Locate every Plasmodium falciparum-infected red blood cell.
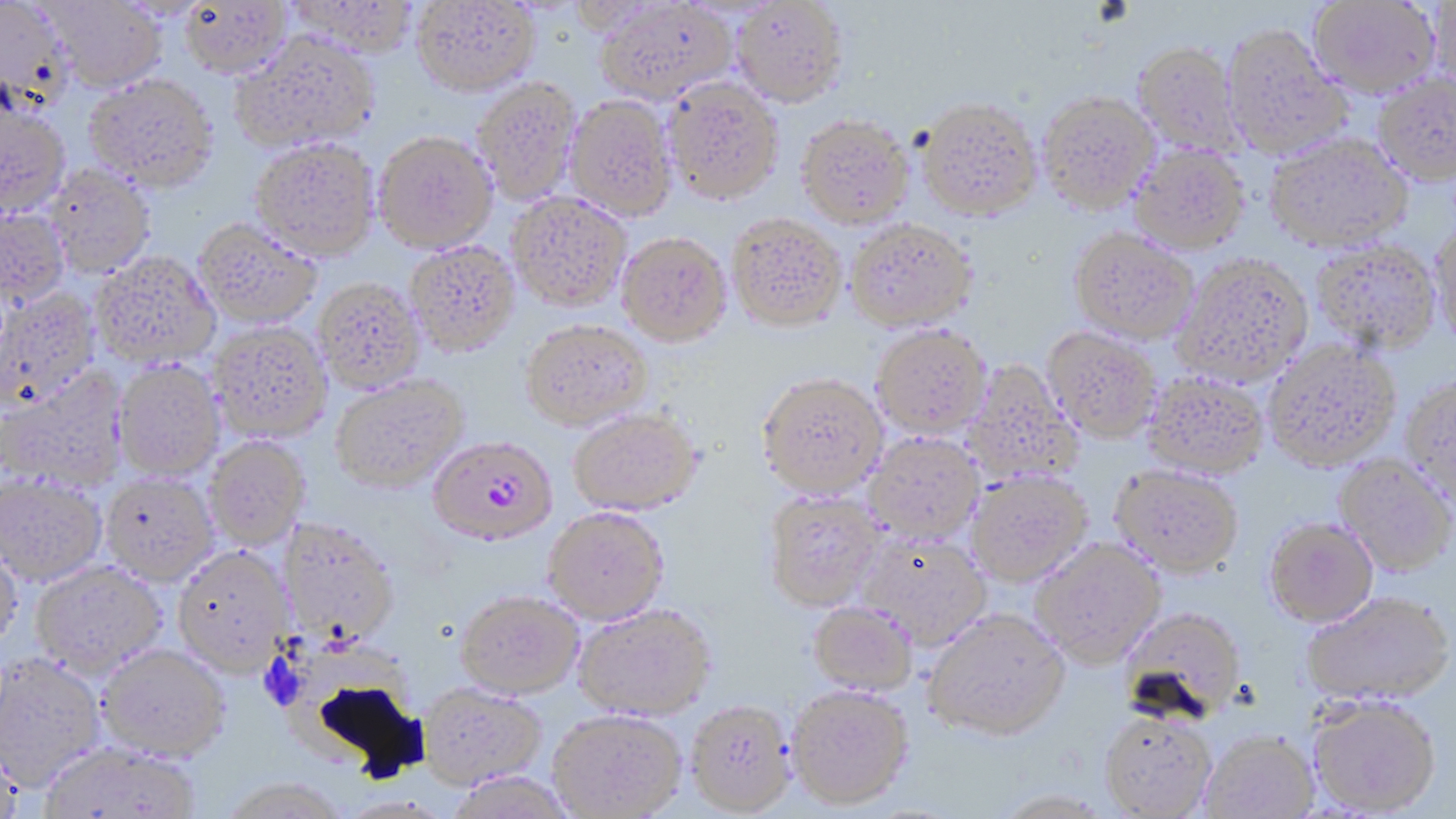

Approximate bounding boxes as (x1, y1, x2, y2) in pixels.
Plasmodium falciparum-infected red blood cells: (429, 438, 558, 548).

Summary:
  - Uninfected red blood cell locations: (0, 0, 71, 111), (44, 0, 168, 92), (286, 0, 420, 58), (411, 0, 540, 95), (1308, 0, 1441, 97), (179, 1, 291, 77), (596, 1, 736, 104), (732, 1, 849, 107), (1428, 1, 1456, 97), (1220, 24, 1353, 159), (231, 31, 380, 153), (1132, 42, 1244, 157), (1373, 73, 1456, 185), (84, 74, 218, 191), (472, 77, 580, 206), (664, 78, 784, 204), (1037, 90, 1159, 213), (565, 96, 676, 221), (917, 96, 1043, 221), (0, 100, 70, 217), (796, 115, 914, 229), (373, 133, 497, 255), (1265, 133, 1413, 253), (251, 139, 380, 262), (1129, 145, 1251, 255), (45, 163, 155, 278), (507, 192, 632, 312), (0, 209, 69, 307), (727, 216, 847, 333), (193, 220, 321, 329), (846, 220, 978, 332), (1430, 222, 1456, 350), (1069, 229, 1199, 344), (617, 234, 732, 347), (405, 241, 520, 357), (1311, 241, 1441, 353), (92, 253, 220, 370), (1173, 255, 1313, 386), (314, 279, 426, 394), (0, 289, 101, 411), (520, 321, 654, 432), (208, 323, 332, 443), (871, 325, 992, 440), (1043, 327, 1162, 443), (1263, 340, 1401, 469), (960, 361, 1083, 488), (113, 362, 225, 482), (1, 371, 129, 492), (1144, 371, 1269, 478), (756, 375, 887, 500), (331, 376, 468, 495), (1401, 376, 1456, 506), (569, 409, 702, 516), (863, 433, 984, 545), (204, 438, 310, 551), (1334, 454, 1456, 576), (1110, 464, 1245, 577), (966, 470, 1092, 586), (0, 475, 106, 587), (101, 475, 217, 586), (764, 492, 884, 612), (543, 508, 670, 626), (1263, 517, 1378, 627), (279, 520, 400, 647), (856, 534, 991, 650), (1030, 537, 1165, 668), (0, 540, 24, 655), (173, 548, 293, 678), (31, 562, 166, 682), (1302, 591, 1455, 707), (456, 592, 582, 699), (808, 601, 918, 697), (573, 606, 715, 722), (1120, 606, 1247, 724), (923, 610, 1071, 741), (96, 644, 230, 762), (0, 654, 106, 792), (418, 684, 546, 792), (787, 687, 915, 812), (1307, 695, 1442, 815), (686, 702, 796, 817), (548, 711, 686, 819), (1099, 712, 1218, 817), (1201, 731, 1319, 818), (0, 741, 26, 819), (37, 743, 203, 819), (446, 773, 577, 819), (218, 780, 350, 819)
  - Slide-level diagnosis: Plasmodium falciparum
  - Preparation: thin blood film
  - Image size: 1456×819 pixels
  - Field of view: one of a larger specimen
  - Stain: May-Grünwald-Giemsa
  - Modality: optical microscopy
  - Magnification: 1000x